Assess the morphology of the red blood cells.
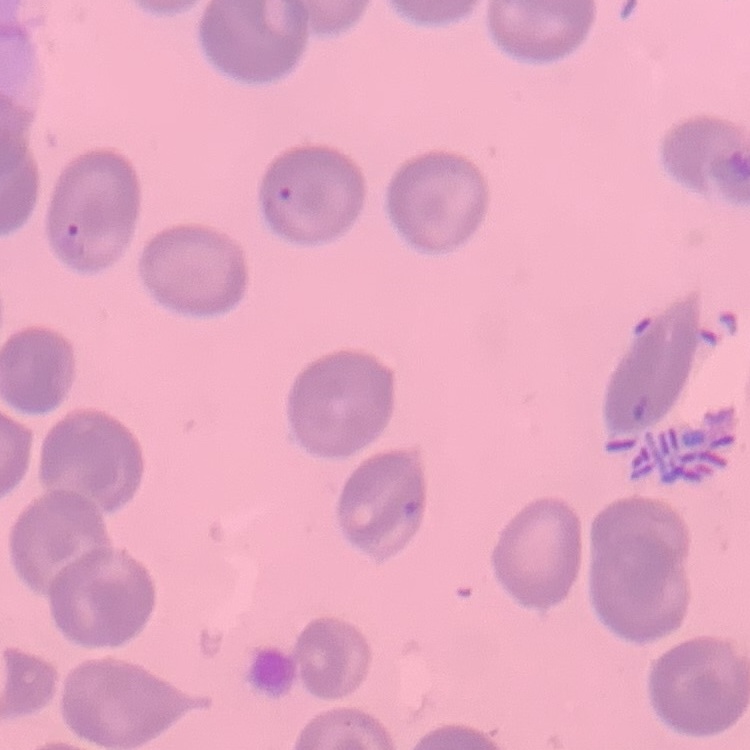

They show no rouleaux formation.

Summary:
  - Preparation: thin blood film
  - Image type: one tile cut from a larger photomicrograph
  - Stain: Field's or Giemsa